Name the parasite shown.
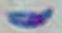

This is Toxoplasma gondii.

Summary:
  - Magnification: 1000x
  - Modality: micrograph